Point out each Plasmodium parasite.
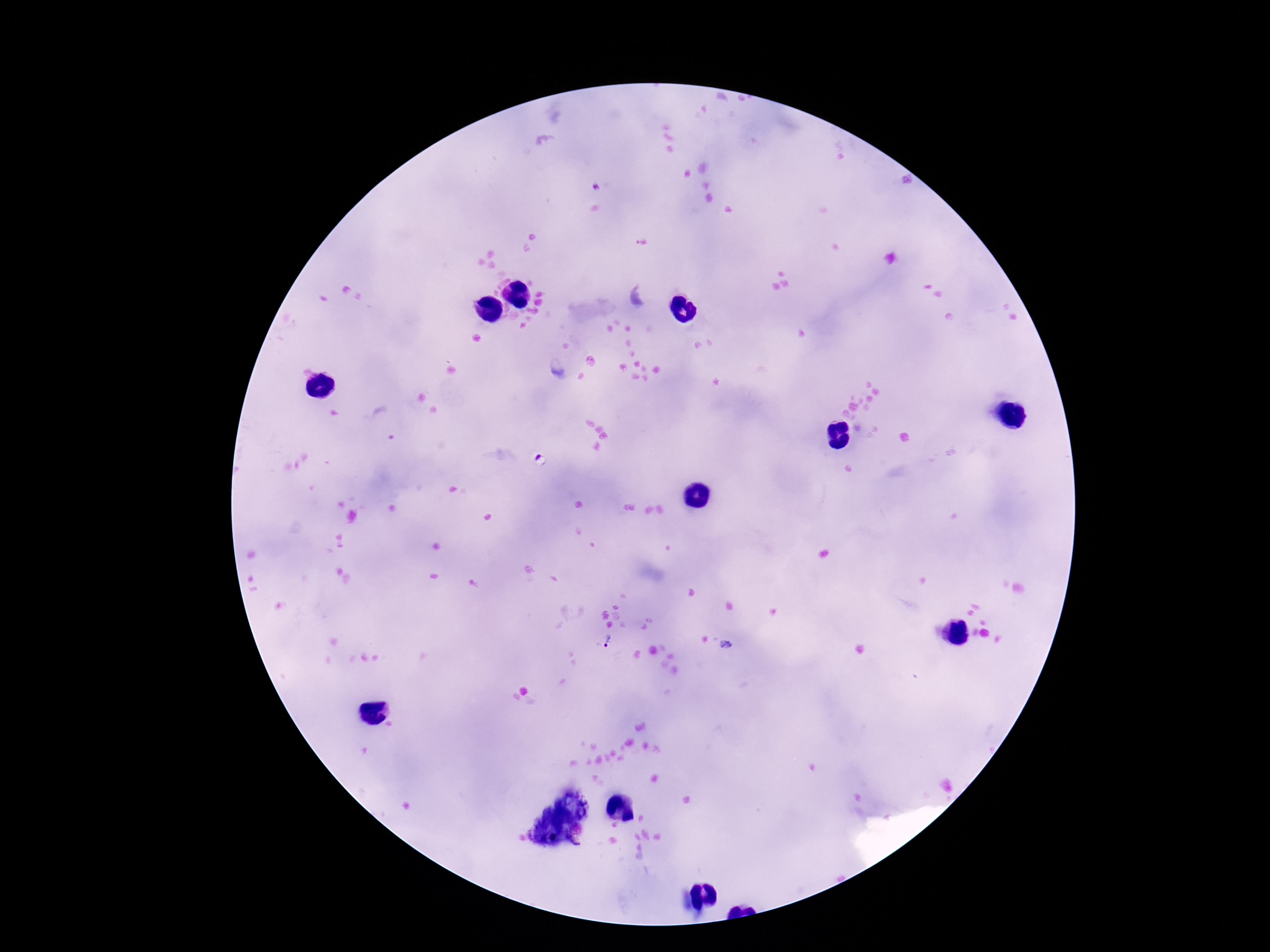
Approximate centers as {x, y} in pixels.
Plasmodium parasites: {381, 424}, {542, 460}, {603, 640}, {726, 645}.

stain: Giemsa
field_of_view: one from this slide
magnification: 100x
image_size: 1270×952 pixels
capture: smartphone camera through the microscope eyepiece
preparation: thick blood film
patient_malaria_status: infected